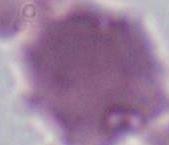
An erythrocyte is shown. 1000x magnification. Photomicrograph.